Identify the parasite.
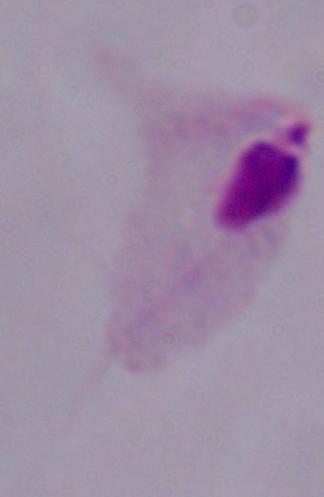
This is a trichomonad.

modality: photomicrograph
magnification: 1000x